Give the position of every Plasmodium parasite.
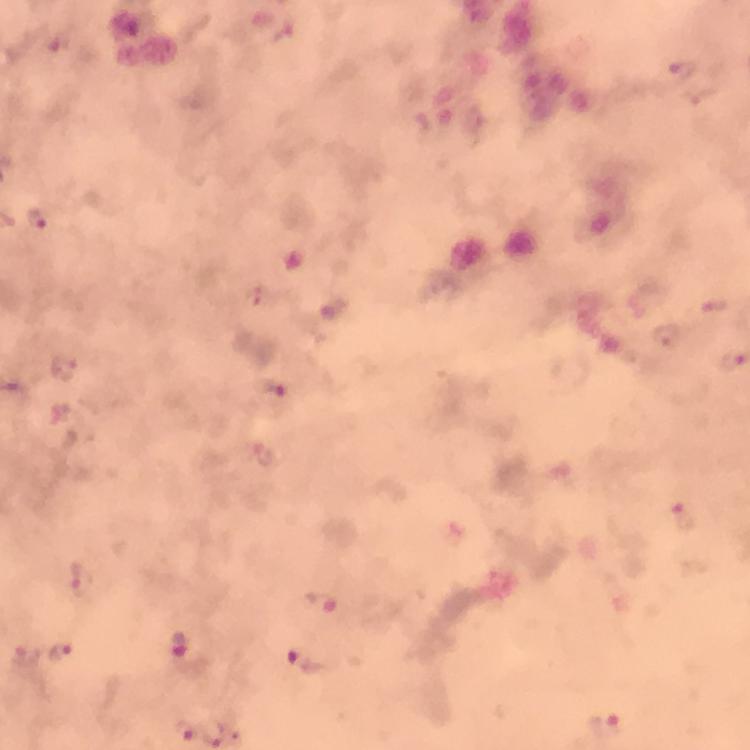

Approximate centers as {x, y} in pixels.
Plasmodium parasites: {37, 219}, {667, 336}, {67, 369}, {272, 391}, {682, 517}, {85, 581}, {320, 603}, {183, 646}, {61, 650}, {308, 661}, {606, 725}, {184, 731}.

Summary:
  - Preparation: thick smear
  - Immersion oil: applied
  - Image size: 750×750 pixels
  - Capture: smartphone camera through the microscope
  - Context: from a malaria diagnostic workup
  - Magnification: 100x
  - Cropped from: one field of view
  - Stain: Giemsa